Locate every Babesia divergens-infected red blood cell.
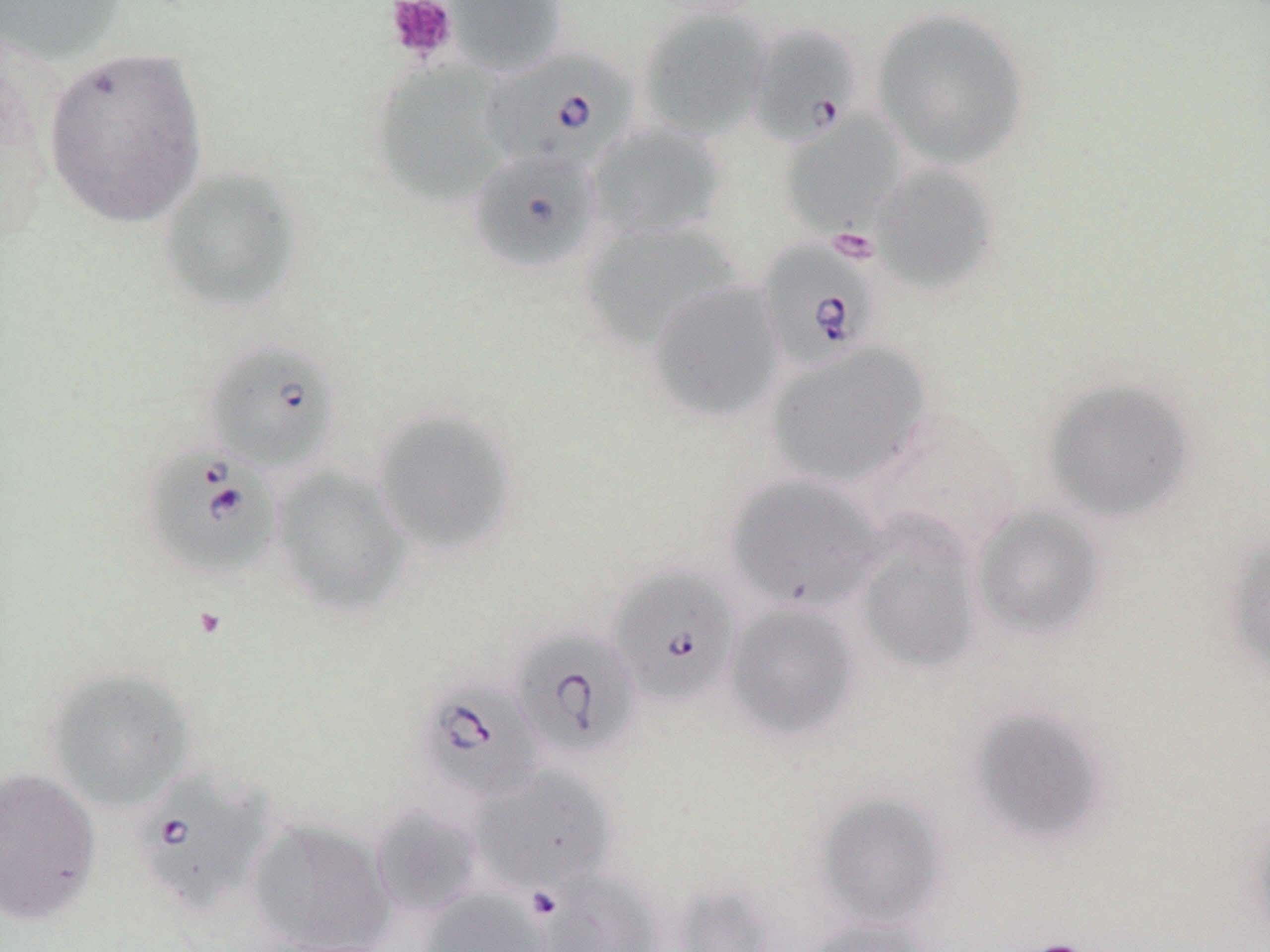
Approximate bounding boxes as [x1, y1, x2, y2] in pixels.
Babesia divergens-infected red blood cells: [749, 23, 863, 148], [482, 48, 638, 176], [467, 149, 603, 273], [757, 237, 884, 371], [204, 340, 340, 474], [141, 444, 282, 581], [607, 565, 740, 708], [510, 627, 642, 760], [416, 678, 546, 804], [132, 765, 273, 917].

Platelet locations: [384, 0, 458, 64], [1019, 939, 1095, 952]. Uninfected red blood cell locations: [0, 0, 128, 66], [442, 0, 568, 78], [870, 6, 1030, 170], [637, 9, 772, 141], [42, 44, 209, 228], [371, 60, 512, 210], [779, 112, 905, 236], [587, 123, 726, 240], [869, 163, 999, 294], [157, 166, 302, 313], [580, 222, 743, 349], [647, 280, 785, 423], [764, 342, 932, 490], [1041, 377, 1197, 523], [373, 407, 518, 556], [862, 408, 1026, 561], [270, 466, 413, 617], [725, 474, 887, 612], [971, 505, 1106, 641], [854, 521, 983, 675], [1222, 534, 1270, 684], [723, 603, 862, 741], [43, 666, 196, 812], [967, 706, 1111, 847], [470, 765, 617, 893], [0, 767, 101, 926], [813, 791, 948, 930], [370, 803, 485, 918], [1242, 811, 1270, 947], [246, 819, 394, 952], [534, 870, 663, 952], [418, 887, 551, 951], [801, 917, 934, 952]. Slide-level diagnosis: Babesia divergens. Light microscopy. 1000x magnification. Image is 1270×952 pixels. Thin blood smear. One field of a larger specimen. May-Grünwald-Giemsa stain.